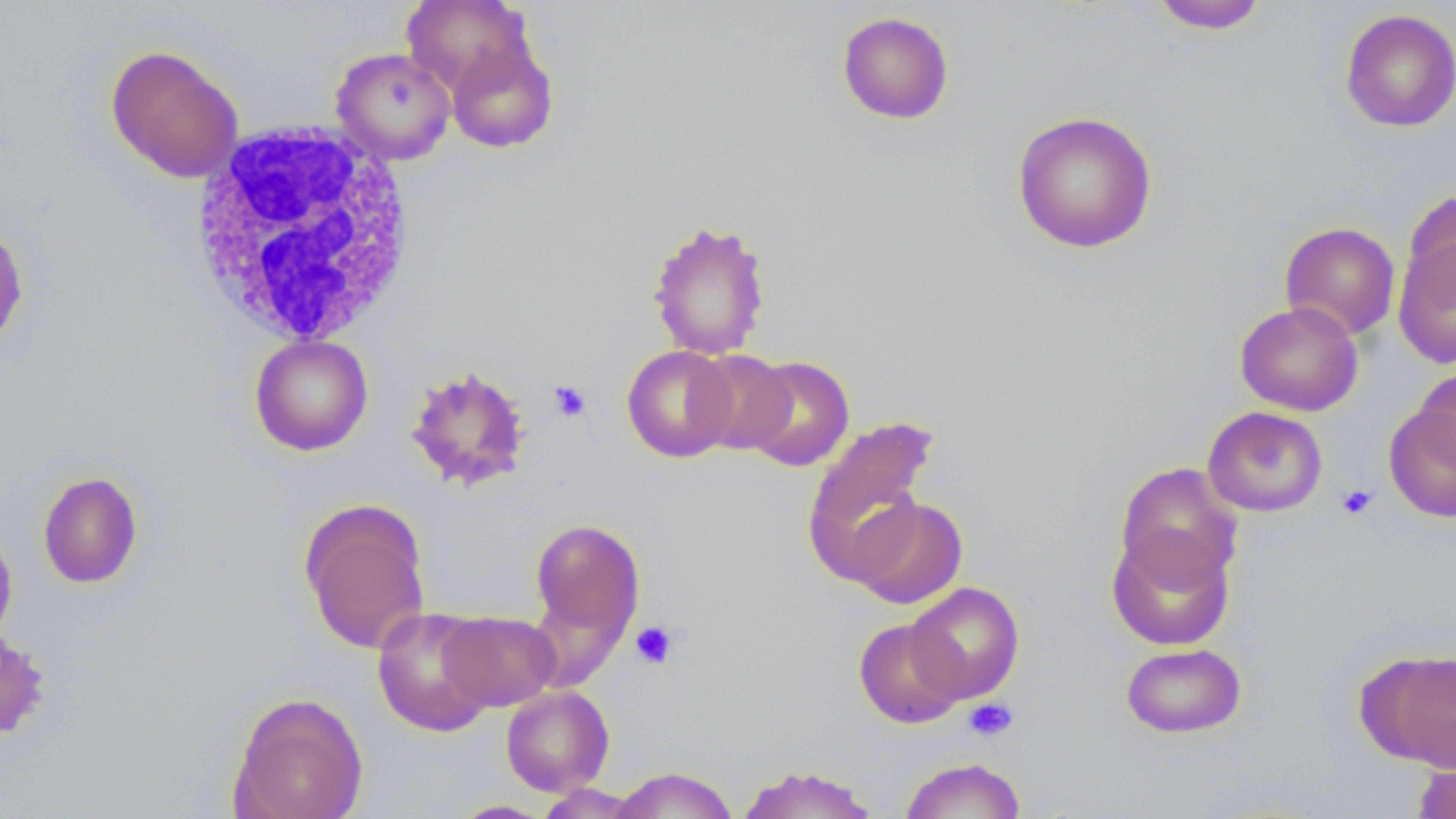
Summary:
  - Coordinate format: approximate bounding boxes as (x1,y1)-(x2,y2) corner pairs in pixels
  - Platelet locations: (548,380)-(592,422), (1336,484)-(1378,520), (630,620)-(680,669), (964,698)-(1018,742)
  - White blood cell locations: (188,120)-(418,348)
  - Uninfected red blood cell locations: (401,0)-(534,97), (1149,1)-(1269,34), (1340,8)-(1456,133), (836,11)-(954,125), (445,37)-(559,154), (105,44)-(244,183), (330,46)-(457,165), (1011,110)-(1158,254), (1401,190)-(1456,312), (647,218)-(772,361), (0,220)-(29,352), (1280,221)-(1401,340), (1393,230)-(1456,368), (1235,300)-(1363,416), (249,334)-(373,456), (621,344)-(739,463), (688,349)-(795,455), (739,355)-(855,472), (404,365)-(534,492), (1412,366)-(1456,476), (1383,402)-(1456,523), (1202,406)-(1328,517), (801,415)-(939,583), (1114,462)-(1244,590), (37,471)-(143,589), (849,495)-(968,609), (298,498)-(431,655), (529,518)-(645,648), (0,524)-(18,649), (1106,526)-(1235,651), (905,581)-(1025,703), (372,606)-(498,736), (439,611)-(560,710), (852,618)-(967,728), (0,629)-(52,743), (1120,642)-(1247,739), (1357,647)-(1456,772), (500,686)-(614,796), (227,691)-(369,819), (899,757)-(1027,819), (1411,758)-(1456,819), (734,765)-(881,819), (611,766)-(739,818), (535,783)-(644,818), (448,799)-(557,818)
  - Slide-level diagnosis: negative for blood parasites
  - Field of view: one of a larger specimen
  - Image size: 1456×819 pixels
  - Modality: optical microscopy
  - Stain: May-Grünwald-Giemsa
  - Magnification: 1000x
  - Preparation: thin blood film